Assess the morphology of the erythrocytes.
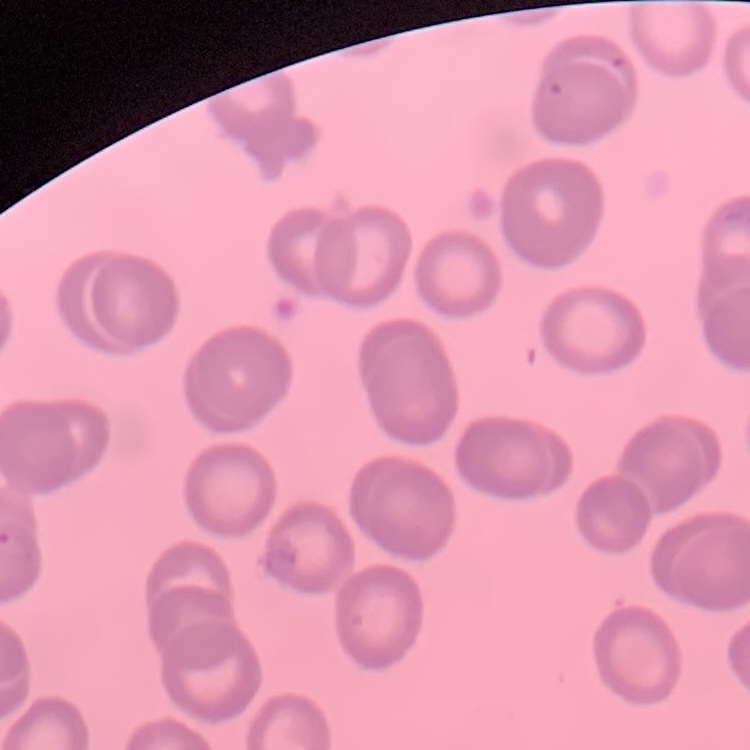
They show no rouleaux formation.

Summary:
  - Stain: Field's or Giemsa
  - Image type: one tile cut from a larger photomicrograph
  - Preparation: thin blood film